Comment on the morphology of the red blood cells.
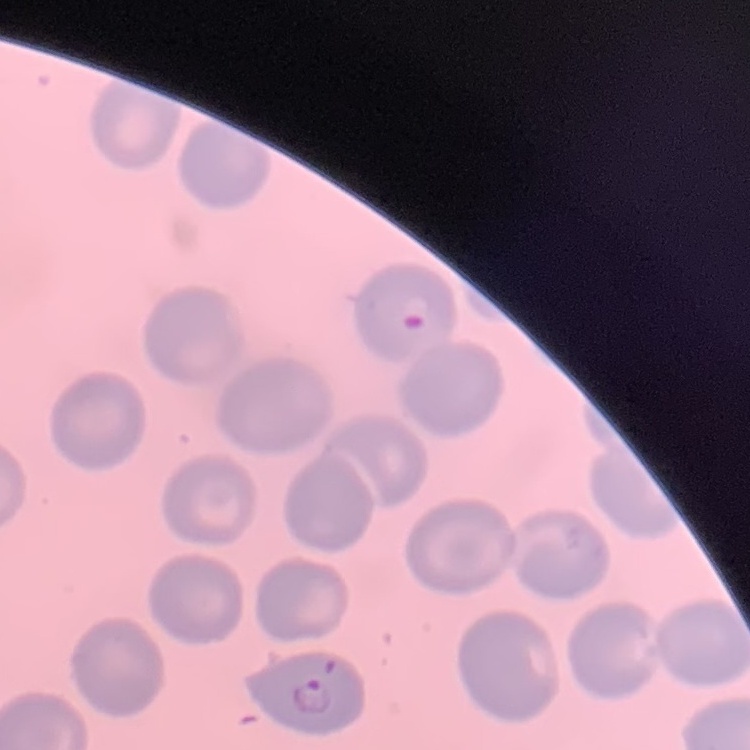

No rouleaux formation.

image type = square crop of a larger photomicrograph
stain = Field's or Giemsa
preparation = thin blood smear